Name the parasite shown.
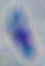

This is Toxoplasma gondii.

1000x magnification. Micrograph.